Look for Plasmodium parasites.
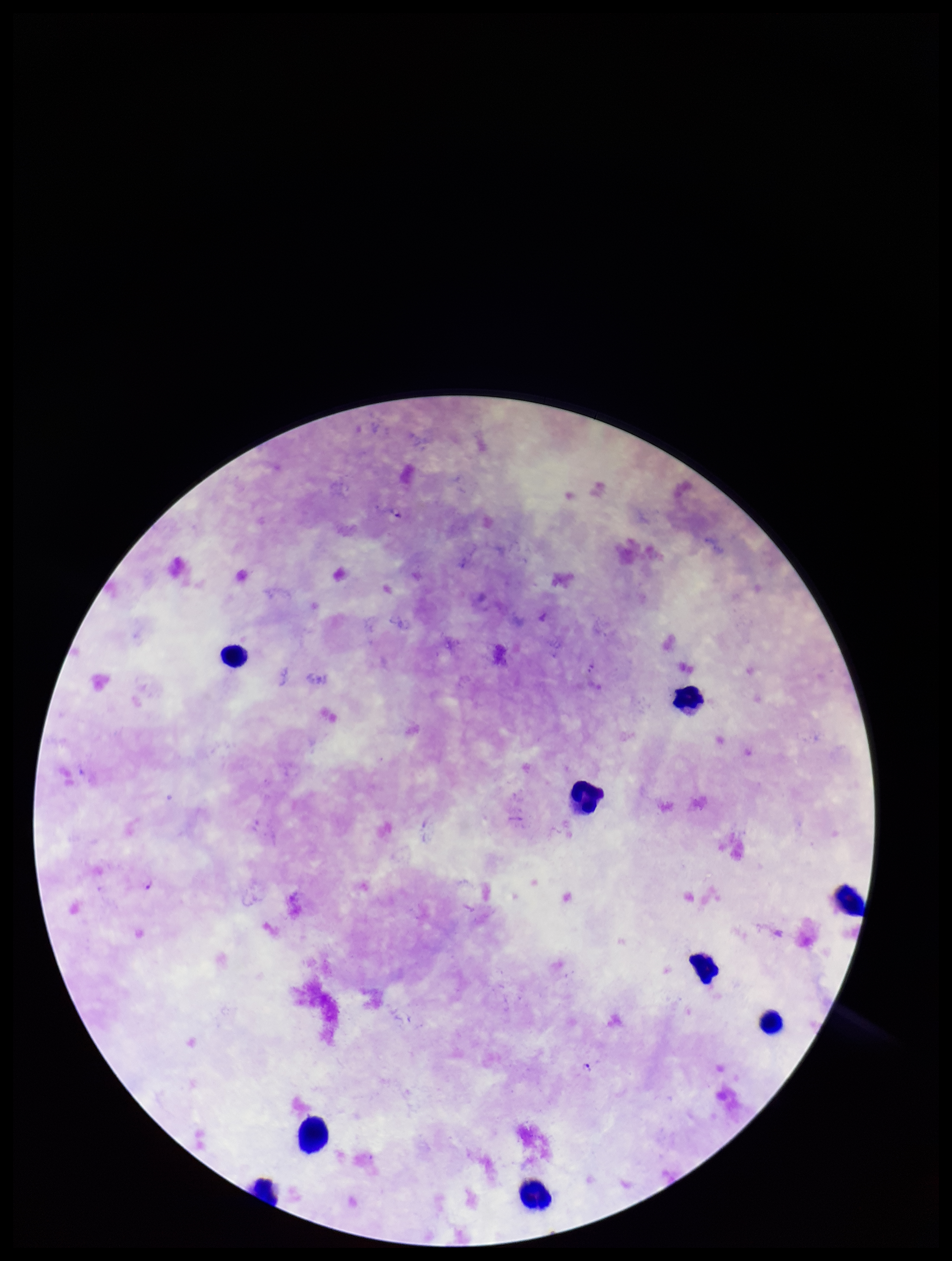

Seen.

species reported for this patient = Plasmodium falciparum
parasite count = 2
patient malaria status = positive
stain = Giemsa
leukocyte count = 9
capture = smartphone photograph through the microscope eyepiece
field of view = one from this slide
image size = 952×1261 pixels
preparation = thick smear